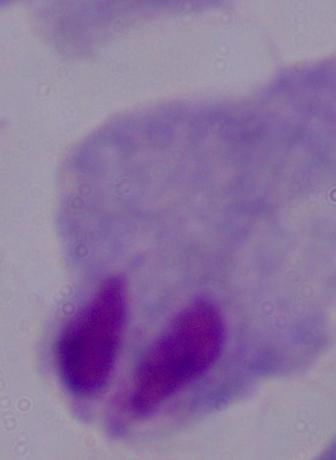
Summary:
  - Identification: trichomonad
  - Modality: photomicrograph
  - Magnification: 1000x